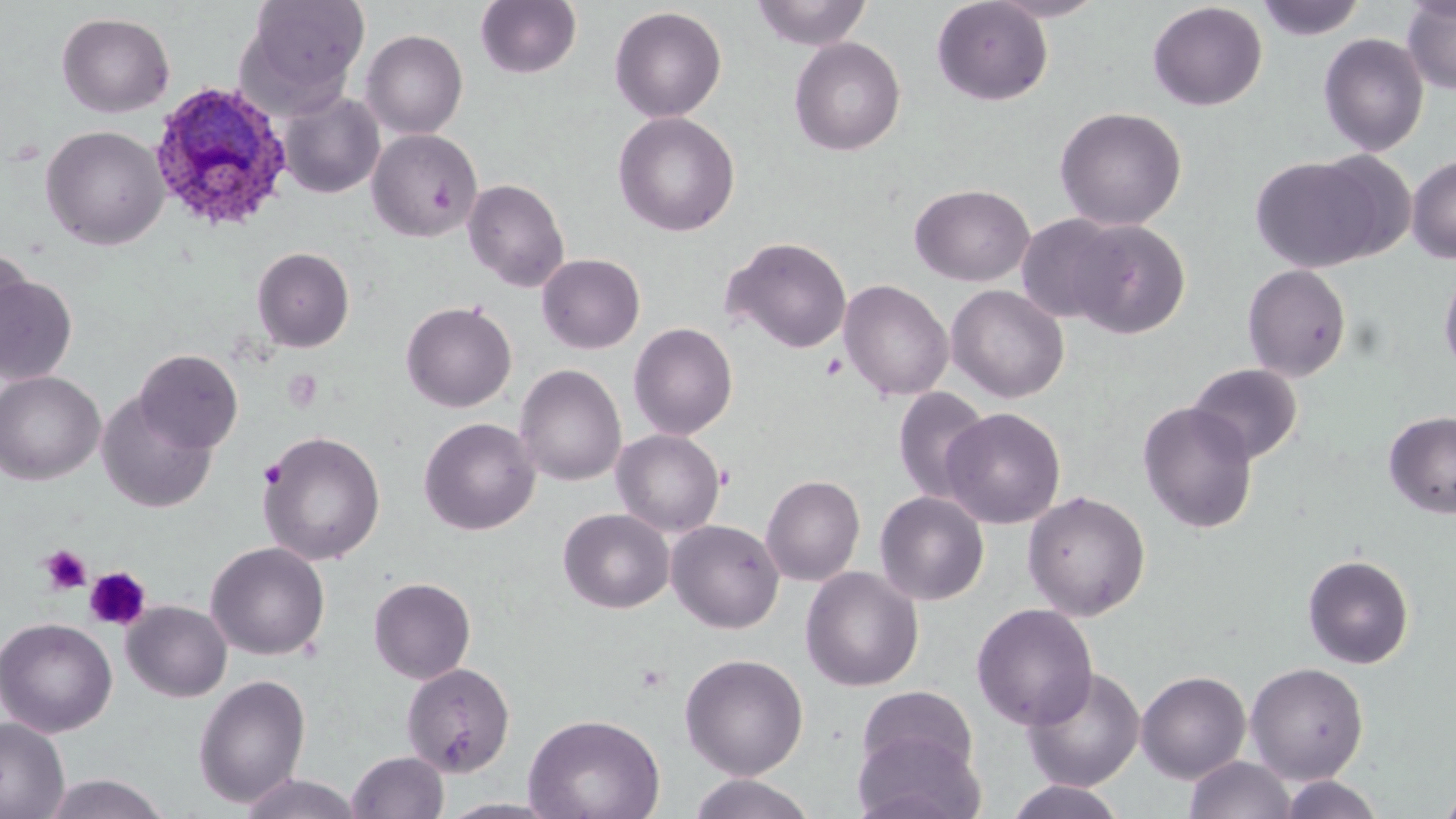
Approximate bounding boxes as named x1/y1/x2/y2 corners in pixels. Uninfected red blood cell locations: (x1=239, y1=0, x2=370, y2=108), (x1=475, y1=0, x2=582, y2=80), (x1=750, y1=0, x2=873, y2=50), (x1=931, y1=0, x2=1054, y2=105), (x1=986, y1=0, x2=1109, y2=22), (x1=1255, y1=0, x2=1367, y2=41), (x1=1401, y1=0, x2=1456, y2=95), (x1=1147, y1=2, x2=1268, y2=111), (x1=609, y1=6, x2=727, y2=122), (x1=56, y1=12, x2=175, y2=118), (x1=360, y1=29, x2=468, y2=139), (x1=1318, y1=33, x2=1429, y2=156), (x1=789, y1=37, x2=906, y2=156), (x1=277, y1=89, x2=385, y2=199), (x1=1054, y1=106, x2=1187, y2=231), (x1=613, y1=111, x2=740, y2=236), (x1=41, y1=125, x2=169, y2=250), (x1=367, y1=129, x2=481, y2=242), (x1=1250, y1=155, x2=1386, y2=274), (x1=1407, y1=155, x2=1456, y2=264), (x1=463, y1=177, x2=570, y2=292), (x1=909, y1=184, x2=1035, y2=287), (x1=1016, y1=215, x2=1126, y2=324), (x1=1068, y1=219, x2=1191, y2=340), (x1=723, y1=236, x2=852, y2=354), (x1=0, y1=246, x2=33, y2=367), (x1=251, y1=247, x2=354, y2=352), (x1=536, y1=253, x2=645, y2=354), (x1=1439, y1=261, x2=1456, y2=383), (x1=1241, y1=264, x2=1352, y2=382), (x1=0, y1=274, x2=79, y2=385), (x1=839, y1=279, x2=954, y2=401), (x1=946, y1=284, x2=1070, y2=403), (x1=401, y1=300, x2=517, y2=413), (x1=628, y1=322, x2=738, y2=440), (x1=134, y1=349, x2=243, y2=453), (x1=1186, y1=363, x2=1303, y2=465), (x1=514, y1=364, x2=627, y2=487), (x1=0, y1=370, x2=105, y2=485), (x1=893, y1=387, x2=991, y2=505), (x1=97, y1=391, x2=217, y2=513), (x1=1137, y1=400, x2=1259, y2=534), (x1=940, y1=407, x2=1066, y2=529), (x1=1384, y1=411, x2=1456, y2=518), (x1=419, y1=417, x2=540, y2=536), (x1=257, y1=429, x2=386, y2=566), (x1=611, y1=429, x2=726, y2=537), (x1=760, y1=474, x2=865, y2=586), (x1=1022, y1=490, x2=1151, y2=621), (x1=875, y1=491, x2=990, y2=606), (x1=558, y1=508, x2=674, y2=613), (x1=666, y1=519, x2=784, y2=633), (x1=205, y1=541, x2=330, y2=661), (x1=1302, y1=554, x2=1415, y2=669), (x1=800, y1=566, x2=924, y2=692), (x1=368, y1=576, x2=476, y2=684), (x1=122, y1=600, x2=233, y2=702), (x1=971, y1=603, x2=1098, y2=731), (x1=0, y1=616, x2=117, y2=737), (x1=679, y1=652, x2=809, y2=779), (x1=1245, y1=661, x2=1368, y2=782), (x1=401, y1=662, x2=516, y2=778), (x1=1022, y1=665, x2=1146, y2=792), (x1=1136, y1=670, x2=1251, y2=782), (x1=192, y1=673, x2=312, y2=808), (x1=853, y1=686, x2=982, y2=787), (x1=524, y1=713, x2=665, y2=819), (x1=0, y1=717, x2=69, y2=819), (x1=852, y1=726, x2=986, y2=819), (x1=346, y1=751, x2=449, y2=819), (x1=1184, y1=756, x2=1295, y2=819), (x1=237, y1=772, x2=364, y2=818), (x1=39, y1=773, x2=173, y2=819), (x1=686, y1=773, x2=818, y2=818), (x1=1275, y1=775, x2=1386, y2=818), (x1=1004, y1=779, x2=1129, y2=819), (x1=1436, y1=782, x2=1456, y2=818), (x1=435, y1=797, x2=565, y2=818). Plasmodium ovale-infected red blood cell locations: (x1=147, y1=81, x2=294, y2=234). Platelet locations: (x1=428, y1=181, x2=455, y2=212), (x1=819, y1=352, x2=848, y2=381), (x1=258, y1=459, x2=288, y2=488), (x1=40, y1=544, x2=91, y2=594), (x1=85, y1=566, x2=151, y2=631). Slide-level diagnosis: Plasmodium ovale. Light microscopy. May-Grünwald-Giemsa-stained preparation. Image is 1456×819 pixels. Thin blood film. 1000x magnification. Single field of view.